State which parasite is depicted.
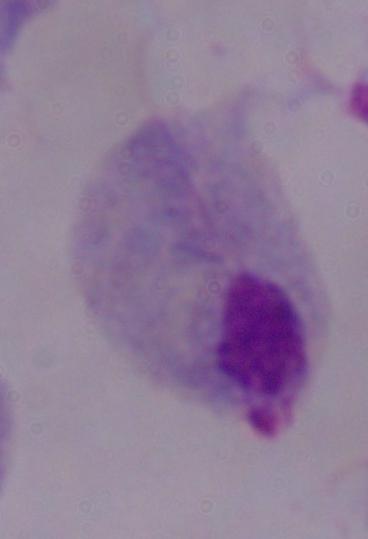
A trichomonad.

magnification = 1000x
modality = micrograph